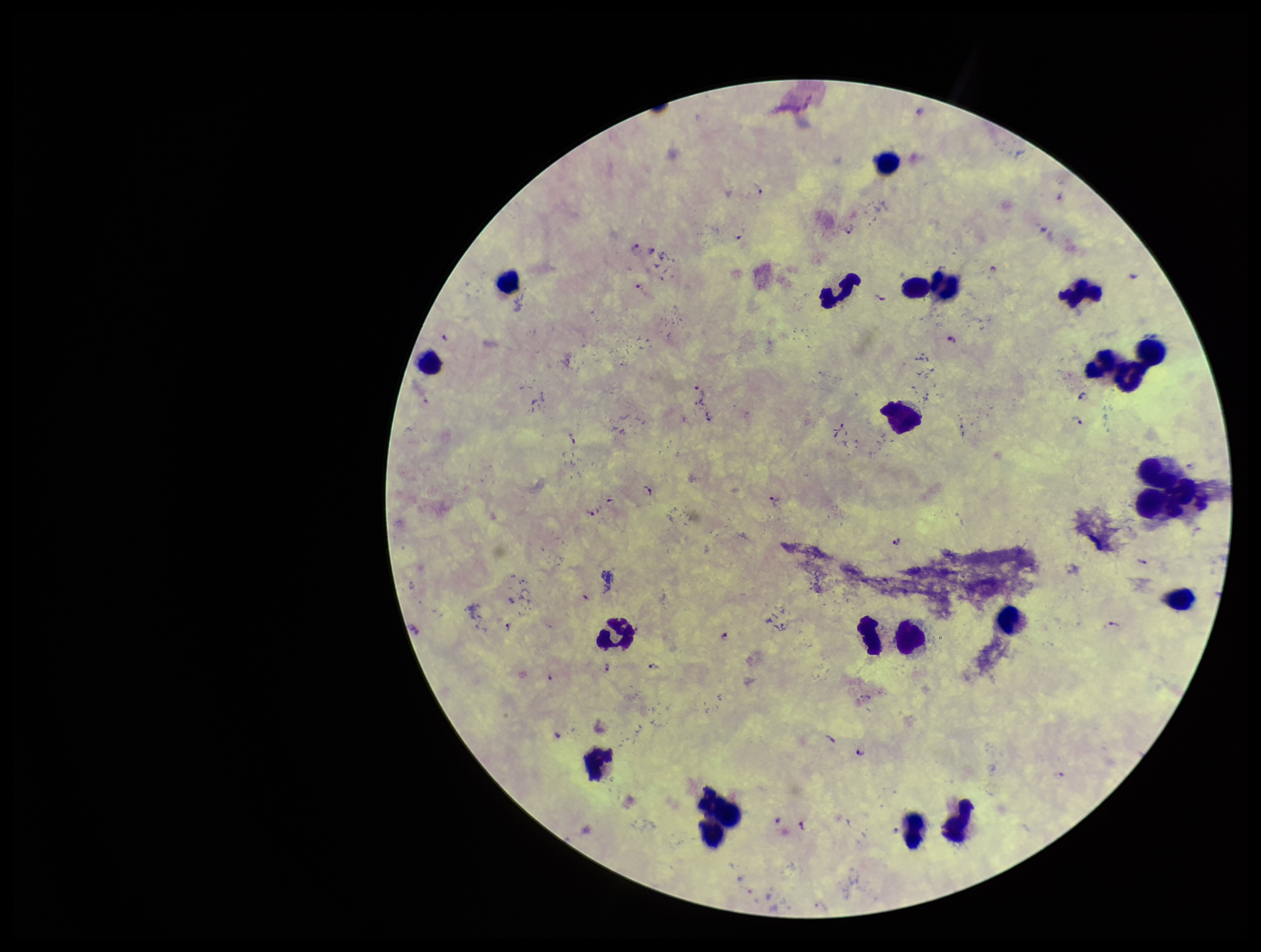

Summary:
  - Parasite count: 31
  - Stain: Giemsa
  - Plasmodium parasites: detected
  - Species reported for this patient: Plasmodium falciparum
  - Capture: smartphone photograph through the microscope eyepiece
  - Leukocyte count: 19
  - Field of view: one from this slide
  - Patient malaria status: infected
  - Preparation: thick blood smear
  - Image size: 1261×952 pixels